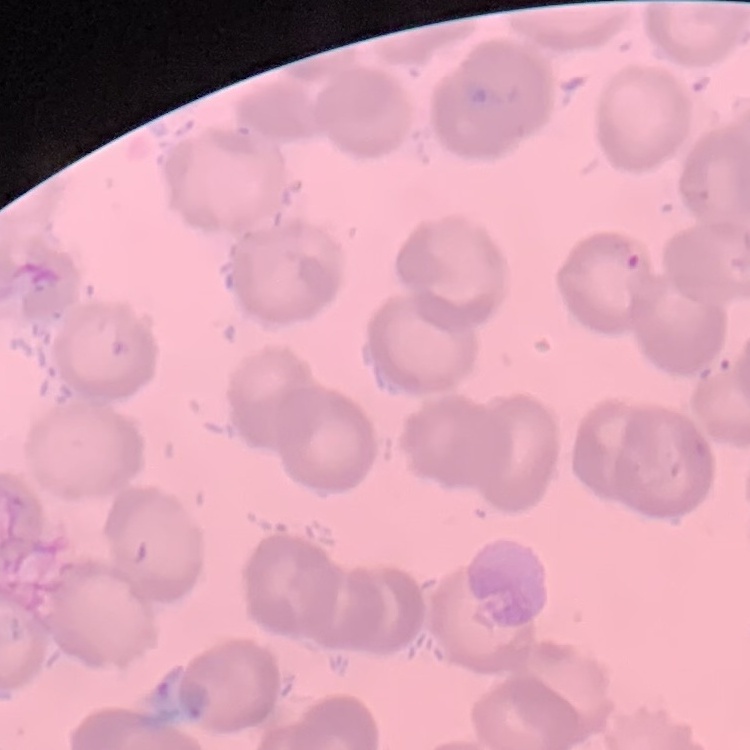
red blood cell morphology = no rouleaux formation
image type = square crop of a larger photomicrograph
stain = Field's or Giemsa
preparation = thin blood smear